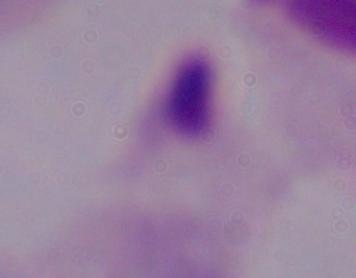
Summary:
  - Modality: photomicrograph
  - Identification: trichomonad
  - Magnification: 1000x